State which parasite is depicted.
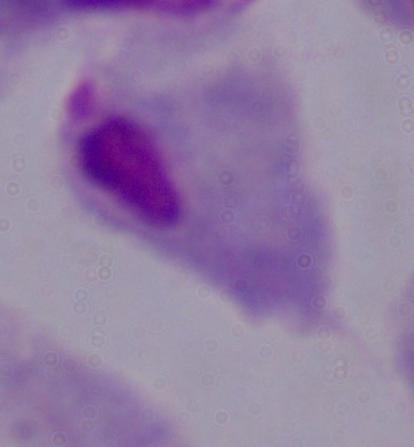
A trichomonad.

modality = photomicrograph
magnification = 1000x